Report the malaria status of this cell.
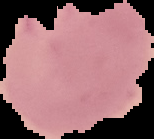

Parasitized.

image type = cell region segmented out of the field of view; surrounding area masked to black
preparation = thin blood smear
image size = 154×139 pixels